Give the position of every malaria parasite.
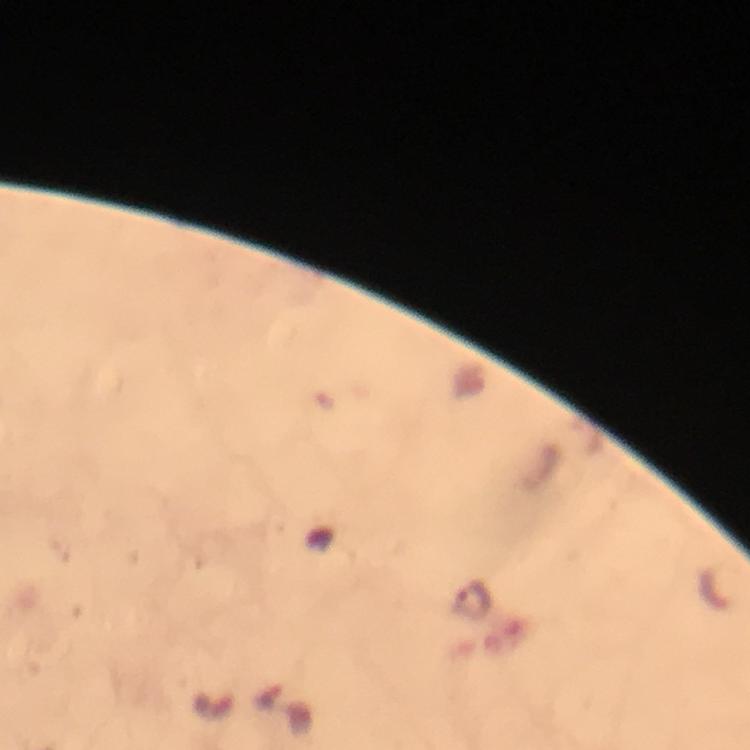

Approximate object centers, in pixels from the top-left corner.
Malaria parasites: (x=473, y=600).

cropped from = a single field of view
immersion oil = applied
image size = 750×750 pixels
stain = Giemsa
context = from a diagnostic examination for malaria
capture = smartphone photograph through a microscope
magnification = 100x
preparation = thick smear